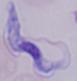

A trypanosome is seen. Micrograph. 1000x magnification.